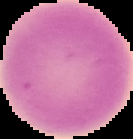

From a thin blood film. Cell region segmented out of the field of view; the surrounding area is masked to black. Image is 133×139 pixels. Result: no malaria parasites seen.